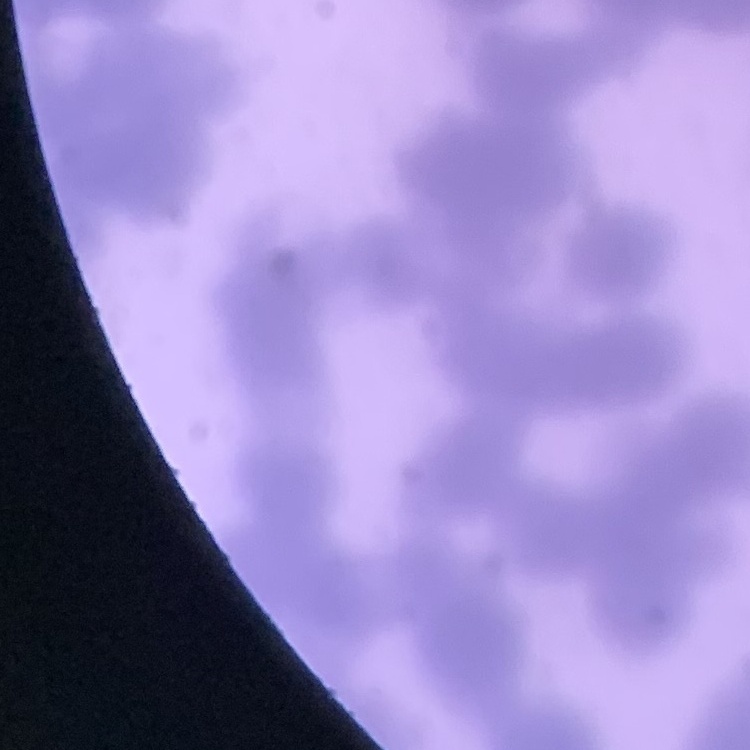
The red blood cells show rouleaux formation. Field's or Giemsa stain. Thin blood film. One tile cut from a larger photomicrograph.